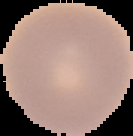

Summary:
  - Result: negative for malaria parasites
  - Preparation: thin blood film
  - Image size: 133×136 pixels
  - Image type: segmented cell region on a black background